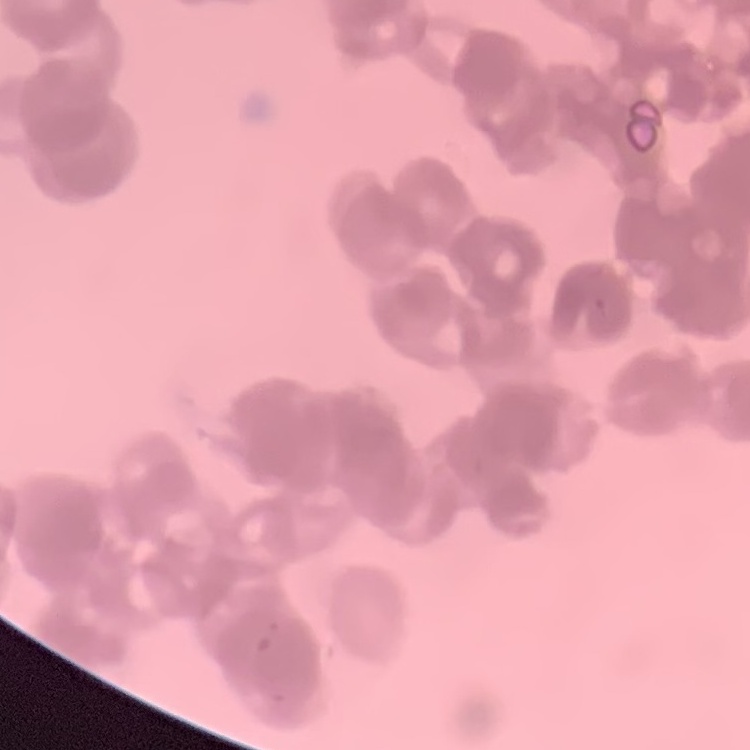
The erythrocytes exhibit rouleaux formation. Thin blood smear. One tile cut from a larger photomicrograph. Stained with either Field's or Giemsa.